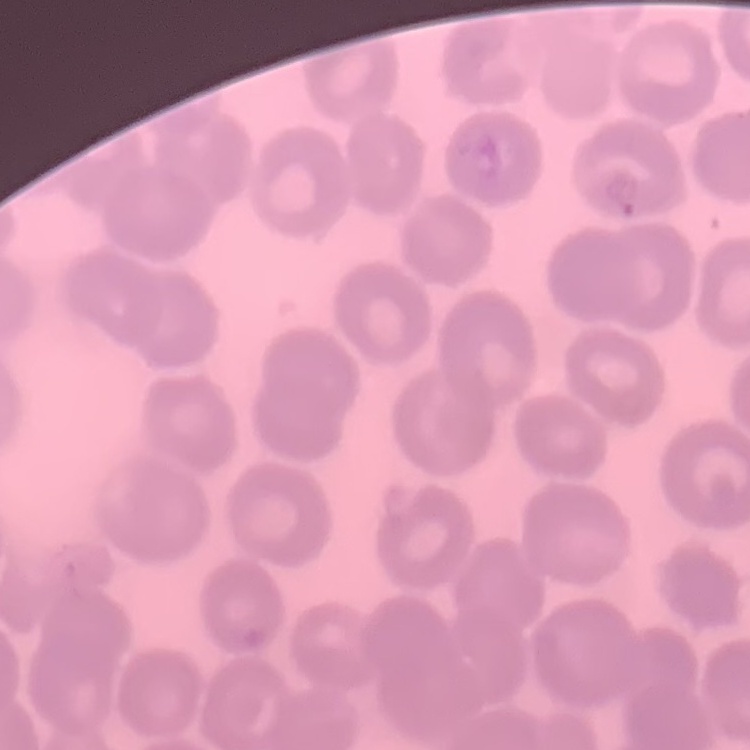

The red blood cells show no rouleaux formation. Thin blood smear. Stained with either Field's or Giemsa. Square crop of a larger photomicrograph.